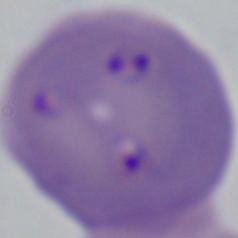
Micrograph. A Babesia parasite is shown. Captured at 1000x magnification.